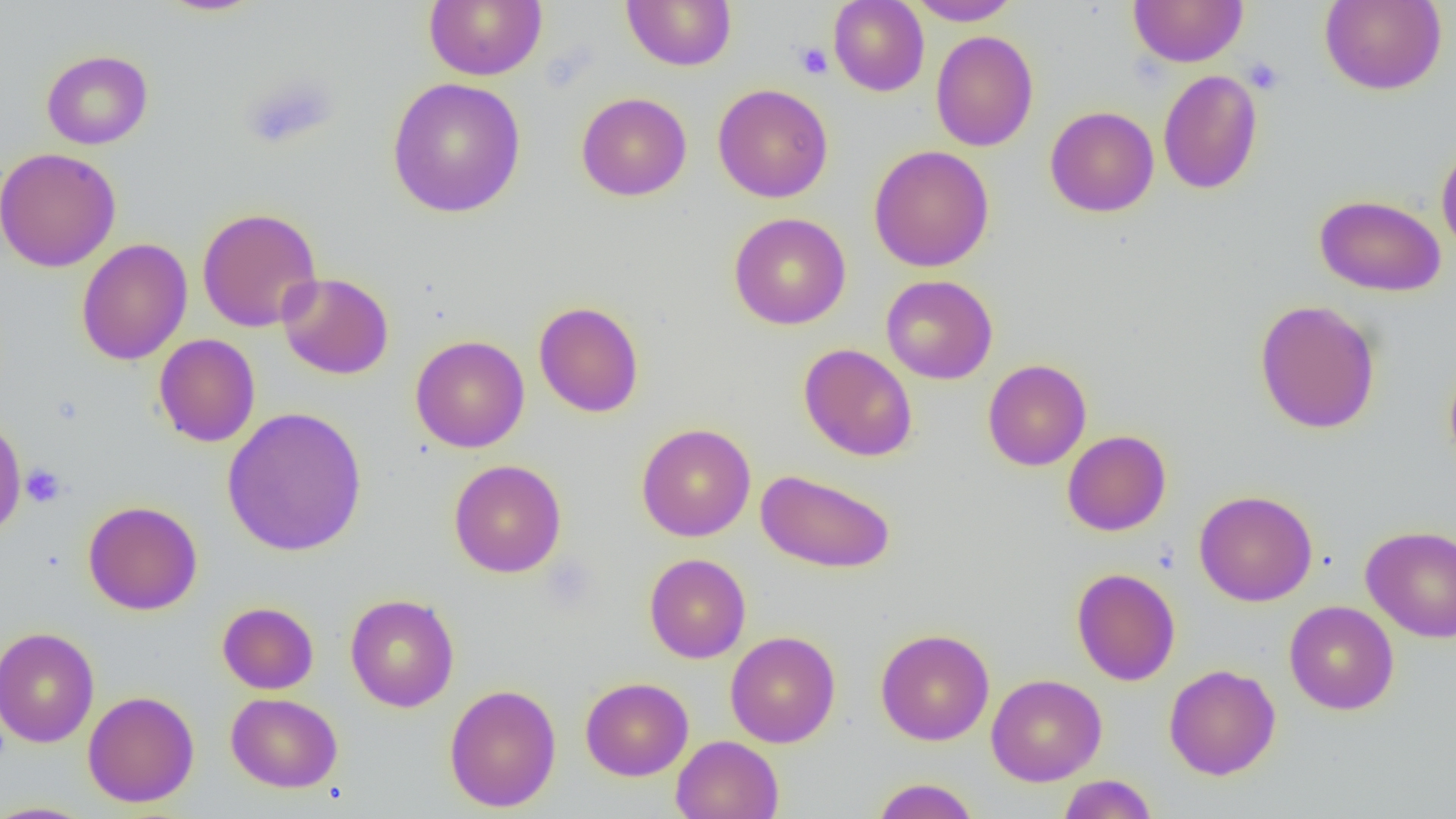
slide-level diagnosis = negative for blood parasites
platelet locations = approximate bounding boxes as (x1, y1, x2, y2) in pixels: (795, 42, 832, 79), (1244, 57, 1285, 95), (240, 73, 339, 150), (21, 464, 66, 507)
field of view = one of a larger specimen
modality = light microscopy
magnification = 1000x
image size = 1456×819 pixels
uninfected red blood cell locations = approximate bounding boxes as (x1, y1, x2, y2) in pixels: (154, 0, 268, 17), (424, 0, 547, 81), (622, 0, 736, 71), (828, 0, 929, 96), (907, 0, 1021, 26), (1128, 0, 1248, 67), (1319, 0, 1447, 95), (930, 30, 1039, 151), (41, 50, 153, 150), (1158, 69, 1263, 195), (387, 77, 526, 218), (713, 83, 833, 203), (576, 92, 692, 201), (1045, 106, 1159, 217), (1436, 139, 1456, 257), (868, 145, 994, 272), (0, 147, 121, 272), (1314, 194, 1446, 297), (197, 207, 322, 332), (729, 212, 851, 330), (77, 238, 192, 365), (277, 272, 393, 379), (881, 274, 998, 384), (1254, 299, 1381, 434), (533, 301, 644, 418), (153, 334, 260, 447), (410, 335, 529, 453), (798, 343, 918, 462), (1443, 356, 1456, 473), (982, 359, 1092, 471), (222, 407, 367, 557), (0, 415, 26, 541), (636, 423, 756, 542), (1062, 430, 1171, 536), (449, 459, 566, 577), (755, 469, 895, 574), (1194, 489, 1318, 606), (83, 500, 202, 615), (1361, 525, 1456, 642), (644, 553, 751, 663), (1071, 568, 1180, 686), (344, 594, 459, 712), (1284, 600, 1399, 715), (217, 601, 319, 694), (0, 626, 99, 749), (876, 628, 994, 746), (724, 630, 840, 748), (1164, 664, 1281, 780), (986, 673, 1107, 786), (580, 677, 693, 781), (444, 684, 561, 812), (83, 690, 199, 807), (226, 692, 343, 792), (671, 735, 784, 818), (1057, 775, 1159, 818), (870, 778, 981, 819), (0, 801, 98, 818)
preparation = thin blood film